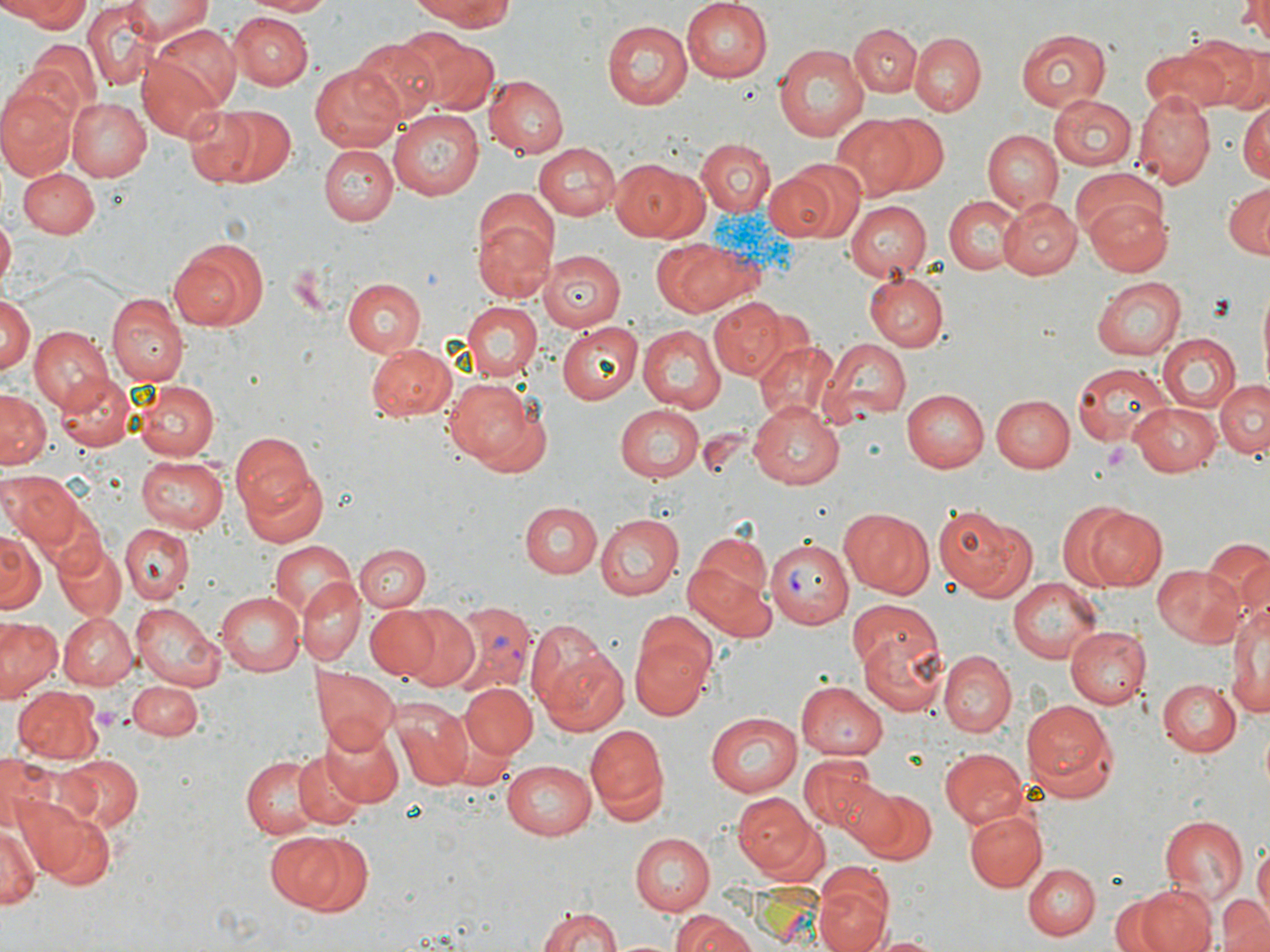

Summary:
  - Coordinate format: approximate bounding boxes as (x1, y1, x2, y2) in pixels
  - Plasmodium vivax-infected red blood cell locations: (763, 538, 852, 630), (446, 603, 537, 696)
  - Uninfected red blood cell locations: (8, 0, 93, 32), (120, 0, 214, 39), (241, 0, 330, 17), (408, 0, 524, 29), (678, 0, 773, 85), (1238, 0, 1270, 45), (83, 4, 154, 87), (233, 13, 310, 89), (601, 21, 692, 109), (147, 23, 241, 114), (850, 23, 922, 99), (1017, 27, 1112, 112), (1187, 31, 1268, 112), (400, 32, 498, 115), (911, 33, 985, 116), (351, 37, 443, 121), (22, 39, 101, 119), (772, 42, 872, 142), (1142, 49, 1226, 115), (138, 56, 228, 142), (310, 62, 404, 152), (487, 74, 568, 157), (0, 87, 74, 179), (1136, 94, 1214, 187), (1048, 95, 1136, 172), (65, 96, 152, 181), (1238, 100, 1270, 182), (190, 102, 296, 188), (390, 110, 484, 199), (873, 114, 951, 196), (830, 115, 921, 200), (981, 129, 1063, 213), (696, 139, 774, 218), (533, 142, 622, 218), (320, 145, 397, 226), (611, 158, 704, 241), (1071, 166, 1165, 244), (17, 167, 99, 237), (762, 169, 841, 242), (1223, 183, 1270, 259), (944, 196, 1021, 275), (997, 196, 1081, 280), (1085, 197, 1173, 275), (844, 202, 931, 280), (0, 216, 15, 286), (474, 216, 557, 304), (166, 236, 269, 331), (655, 237, 758, 318), (542, 249, 625, 331), (865, 273, 949, 351), (1092, 277, 1186, 361), (343, 278, 426, 356), (1255, 281, 1269, 388), (107, 293, 188, 386), (0, 294, 35, 377), (709, 299, 786, 379), (462, 301, 541, 382), (557, 322, 642, 405), (640, 325, 726, 413), (26, 328, 113, 415), (1156, 333, 1241, 412), (819, 339, 910, 421), (363, 342, 456, 423), (754, 342, 842, 427), (1070, 362, 1174, 447), (55, 372, 138, 453), (131, 376, 222, 459), (443, 376, 540, 468), (1214, 379, 1269, 460), (0, 389, 50, 468), (901, 389, 988, 471), (994, 394, 1075, 472), (748, 400, 848, 490), (1129, 400, 1224, 474), (614, 402, 703, 481), (697, 427, 754, 478), (229, 428, 325, 529), (136, 455, 229, 532), (3, 474, 79, 551), (519, 501, 602, 578), (1063, 503, 1168, 592), (935, 506, 1034, 601), (523, 507, 680, 585), (838, 508, 936, 598), (594, 514, 683, 600), (118, 525, 191, 601), (0, 530, 44, 614), (686, 531, 774, 636), (1201, 538, 1270, 625), (52, 539, 127, 622), (268, 541, 358, 623), (355, 544, 429, 611), (1152, 564, 1245, 648), (296, 577, 364, 665), (1008, 577, 1102, 661), (215, 590, 303, 675), (1228, 593, 1269, 728), (845, 598, 938, 682), (136, 603, 221, 689), (392, 603, 482, 693), (363, 606, 443, 680), (61, 612, 137, 690), (0, 617, 62, 697), (525, 618, 611, 712), (629, 619, 717, 721), (1064, 624, 1148, 710), (857, 628, 950, 715), (538, 643, 630, 737), (938, 651, 1016, 737), (313, 667, 399, 752), (1157, 678, 1242, 758), (128, 680, 204, 738), (798, 680, 891, 761), (460, 682, 539, 761), (12, 686, 101, 764), (1022, 698, 1120, 799), (391, 700, 476, 790), (706, 712, 805, 794), (319, 721, 403, 806), (586, 723, 669, 819), (939, 747, 1030, 827), (0, 750, 49, 831), (293, 751, 366, 830), (57, 753, 142, 831), (240, 753, 322, 838), (798, 753, 881, 836), (501, 760, 596, 839), (832, 779, 902, 853), (851, 785, 937, 864), (732, 792, 818, 877), (14, 796, 116, 890), (964, 809, 1047, 893), (1160, 816, 1249, 903), (0, 818, 41, 911), (629, 831, 715, 914), (265, 832, 353, 909), (297, 836, 375, 918), (1254, 843, 1269, 922), (1023, 862, 1099, 939), (814, 878, 893, 952), (1135, 885, 1216, 952), (1110, 896, 1169, 950), (1220, 899, 1270, 952), (533, 903, 628, 952), (669, 912, 761, 952), (867, 932, 945, 952)
  - Platelet locations: (287, 263, 333, 312), (1101, 442, 1137, 474)
  - Slide-level diagnosis: Plasmodium vivax
  - Magnification: 1000x
  - Modality: optical microscopy
  - Stain: May-Grünwald-Giemsa
  - Image size: 1270×952 pixels
  - Preparation: thin blood film
  - Field of view: one of a larger specimen